Describe the morphology of the erythrocytes.
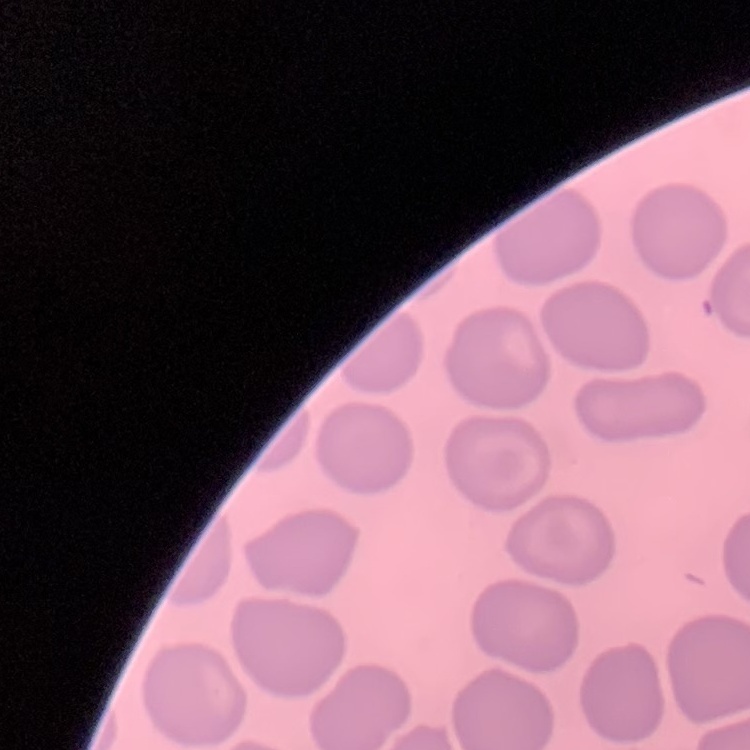
They show no rouleaux formation.

Summary:
  - Image type: square crop of a larger photomicrograph
  - Stain: Field's or Giemsa
  - Preparation: thin blood smear